Name the blood parasite species.
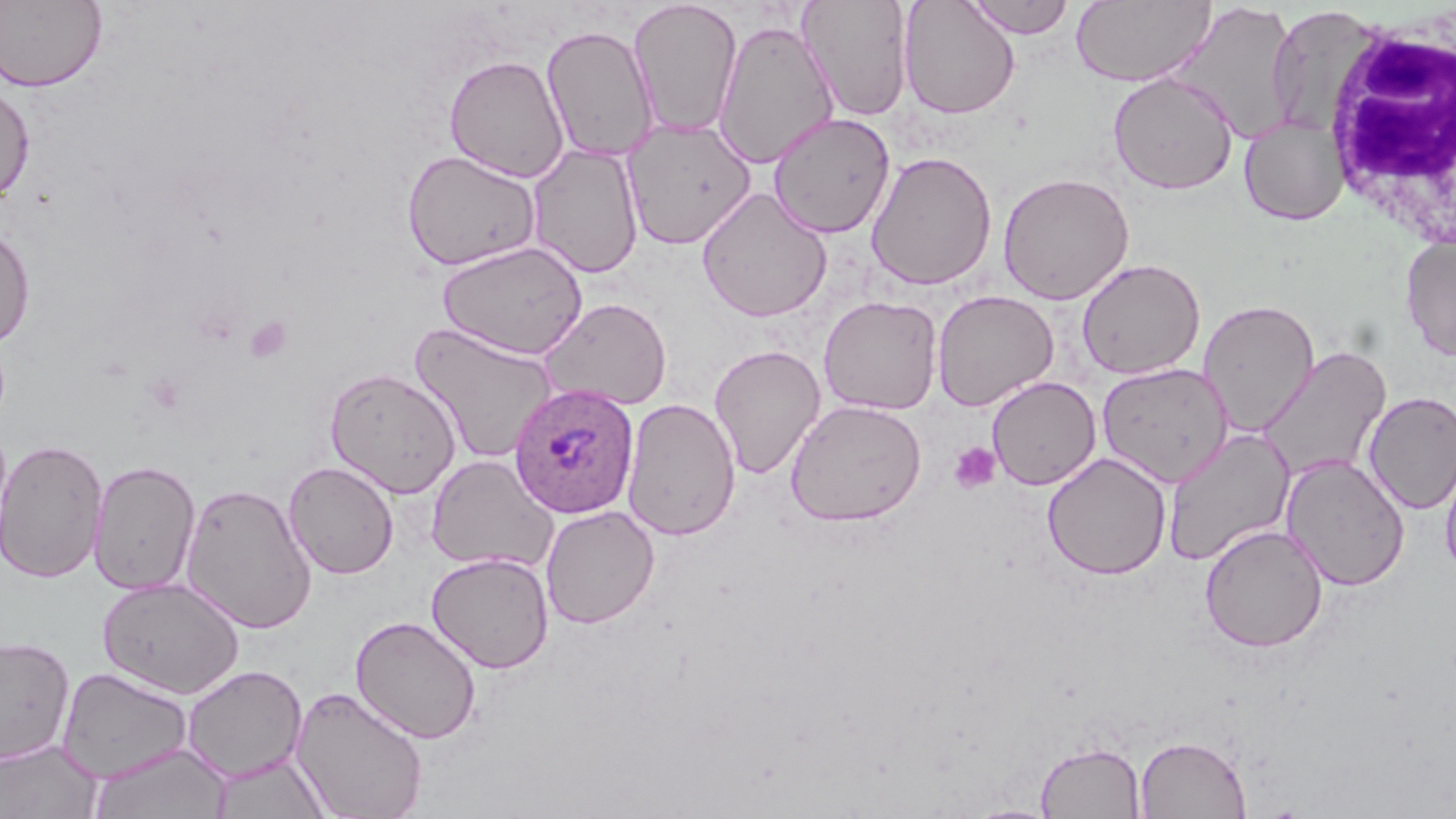

Plasmodium ovale.

Approximate bounding boxes as named x1/y1/x2/y2 corners in pixels. Platelet locations: (x1=244, y1=315, x2=293, y2=365), (x1=948, y1=442, x2=1001, y2=493). White blood cell locations: (x1=1319, y1=9, x2=1456, y2=252). Uninfected red blood cell locations: (x1=0, y1=0, x2=108, y2=93), (x1=799, y1=0, x2=913, y2=121), (x1=964, y1=0, x2=1076, y2=39), (x1=1071, y1=0, x2=1215, y2=87), (x1=629, y1=1, x2=743, y2=139), (x1=898, y1=1, x2=1020, y2=119), (x1=1170, y1=1, x2=1301, y2=144), (x1=1265, y1=5, x2=1379, y2=137), (x1=713, y1=18, x2=839, y2=169), (x1=541, y1=24, x2=659, y2=162), (x1=443, y1=54, x2=569, y2=183), (x1=1108, y1=72, x2=1238, y2=195), (x1=0, y1=79, x2=35, y2=204), (x1=768, y1=112, x2=896, y2=238), (x1=1239, y1=115, x2=1348, y2=226), (x1=621, y1=117, x2=757, y2=248), (x1=527, y1=142, x2=644, y2=279), (x1=401, y1=149, x2=542, y2=271), (x1=866, y1=150, x2=998, y2=291), (x1=997, y1=172, x2=1134, y2=305), (x1=696, y1=187, x2=833, y2=322), (x1=0, y1=226, x2=36, y2=348), (x1=1400, y1=236, x2=1456, y2=361), (x1=439, y1=240, x2=589, y2=360), (x1=1076, y1=258, x2=1206, y2=380), (x1=932, y1=289, x2=1059, y2=411), (x1=818, y1=295, x2=943, y2=415), (x1=539, y1=297, x2=672, y2=411), (x1=1198, y1=299, x2=1320, y2=437), (x1=409, y1=321, x2=560, y2=464), (x1=709, y1=343, x2=826, y2=480), (x1=1256, y1=343, x2=1392, y2=485), (x1=1096, y1=362, x2=1234, y2=487), (x1=324, y1=366, x2=462, y2=498), (x1=987, y1=377, x2=1100, y2=490), (x1=1363, y1=390, x2=1456, y2=514), (x1=621, y1=396, x2=742, y2=541), (x1=785, y1=399, x2=927, y2=526), (x1=1162, y1=426, x2=1296, y2=567), (x1=1, y1=438, x2=109, y2=583), (x1=1439, y1=447, x2=1456, y2=582), (x1=1042, y1=452, x2=1172, y2=580), (x1=425, y1=453, x2=557, y2=573), (x1=1279, y1=454, x2=1411, y2=592), (x1=88, y1=459, x2=201, y2=595), (x1=283, y1=461, x2=399, y2=579), (x1=180, y1=482, x2=317, y2=634), (x1=540, y1=505, x2=660, y2=629), (x1=1199, y1=523, x2=1329, y2=653), (x1=426, y1=551, x2=554, y2=674), (x1=98, y1=576, x2=245, y2=699), (x1=350, y1=615, x2=482, y2=744), (x1=1, y1=635, x2=75, y2=765), (x1=182, y1=664, x2=308, y2=782), (x1=57, y1=667, x2=195, y2=783), (x1=291, y1=685, x2=429, y2=818), (x1=1134, y1=734, x2=1252, y2=818), (x1=0, y1=738, x2=102, y2=818), (x1=1034, y1=741, x2=1147, y2=818), (x1=88, y1=742, x2=233, y2=819), (x1=209, y1=753, x2=333, y2=819), (x1=964, y1=803, x2=1062, y2=819). Plasmodium ovale-infected red blood cell locations: (x1=508, y1=381, x2=640, y2=519). Captured at 1000x magnification. One field of a larger specimen. Thin blood smear. May-Grünwald-Giemsa-stained preparation. Image is 1456×819 pixels. Light microscopy.